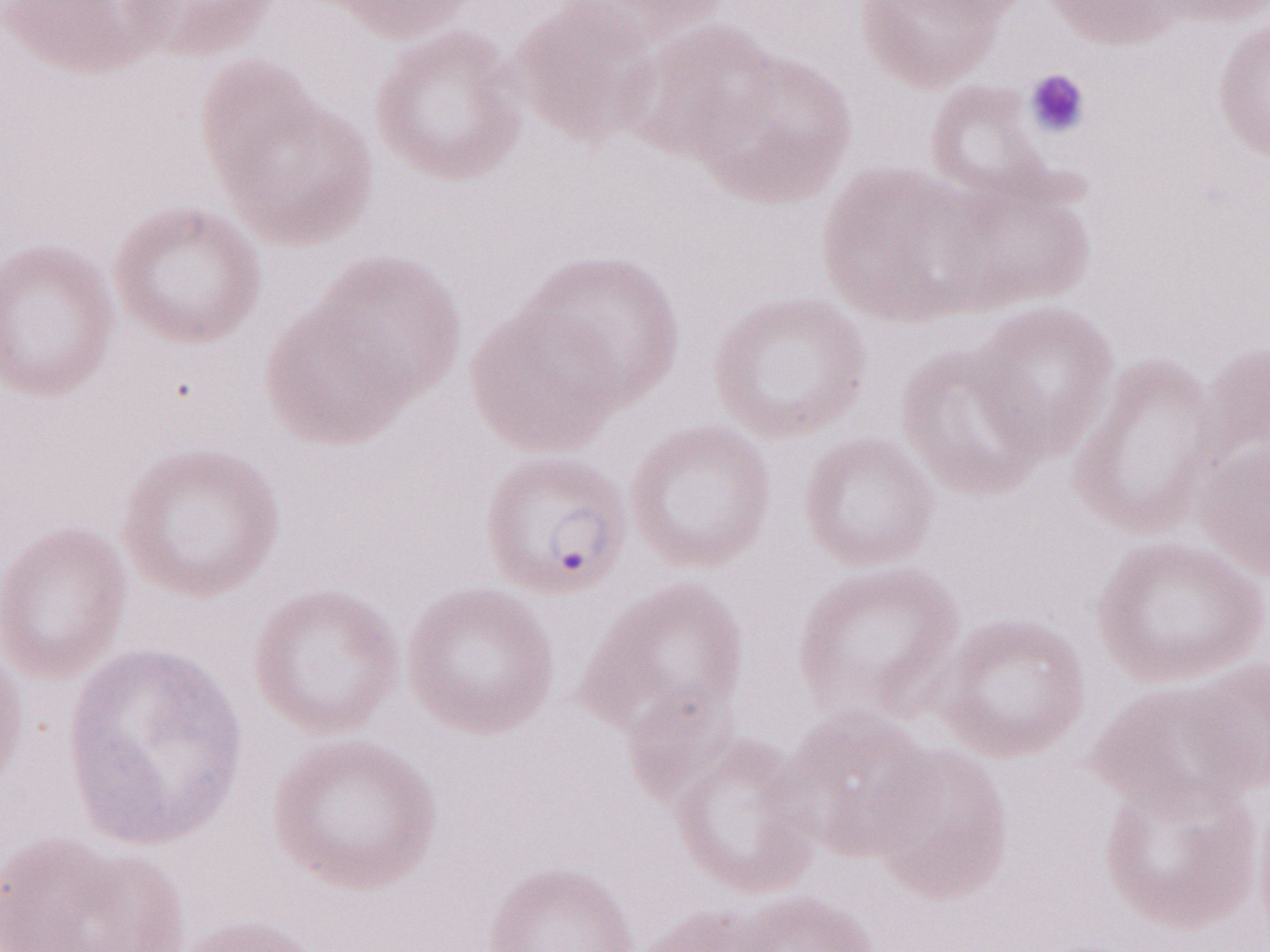
Single field of view. Image is 1270×952 pixels. May-Grünwald-Giemsa stain. Olympus BX43 microscope, Olympus DP73 camera. 1,000x magnification. Thin blood smear. Patient-level malaria diagnosis: positive.